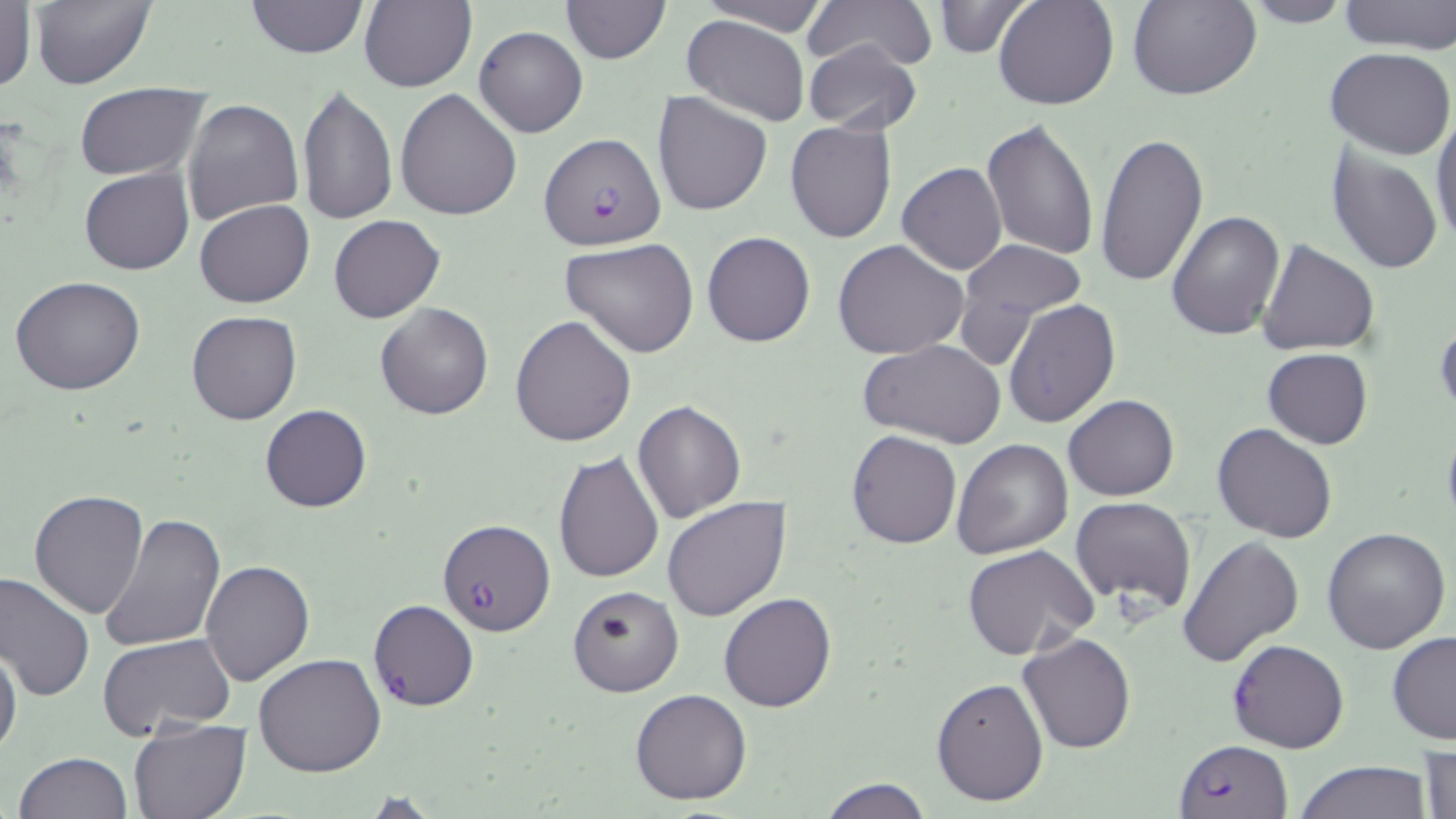

{
  "slide_level_diagnosis": "Plasmodium falciparum",
  "uninfected_red_blood_cell_locations": "approximate bounding boxes as [x1, y1, x2, y2] in pixels: [28, 0, 155, 89], [246, 0, 366, 58], [560, 0, 670, 64], [694, 0, 829, 34], [799, 0, 934, 71], [993, 0, 1119, 110], [1128, 0, 1260, 100], [1336, 0, 1456, 53], [357, 1, 477, 91], [1236, 1, 1356, 28], [0, 2, 36, 94], [930, 2, 1033, 58], [682, 14, 809, 126], [474, 26, 588, 137], [803, 39, 922, 134], [1325, 47, 1456, 161], [74, 82, 209, 182], [296, 82, 397, 226], [395, 88, 521, 221], [651, 91, 773, 216], [183, 98, 307, 226], [1431, 109, 1456, 248], [981, 117, 1099, 261], [785, 118, 898, 245], [1094, 133, 1209, 289], [1326, 148, 1442, 274], [897, 162, 1007, 275], [79, 167, 193, 275], [195, 200, 314, 308], [1167, 211, 1285, 340], [329, 214, 446, 324], [702, 230, 816, 347], [560, 238, 700, 357], [832, 238, 969, 360], [1257, 239, 1381, 355], [958, 240, 1085, 332], [11, 275, 147, 395], [1004, 299, 1122, 431], [375, 302, 493, 419], [186, 310, 302, 426], [510, 315, 639, 447], [1435, 319, 1456, 422], [861, 340, 1007, 449], [1263, 348, 1373, 448], [1063, 395, 1180, 502], [632, 399, 746, 524], [258, 405, 372, 513], [1212, 422, 1338, 543], [1441, 422, 1456, 533], [560, 424, 733, 564], [846, 429, 963, 548], [951, 437, 1075, 558], [554, 450, 665, 582], [28, 489, 148, 619], [662, 496, 792, 623], [1069, 496, 1197, 616], [99, 512, 226, 653], [1320, 527, 1450, 655], [1177, 533, 1305, 668], [963, 546, 1097, 662], [201, 558, 315, 686], [0, 572, 96, 701], [566, 583, 682, 697], [718, 592, 837, 711], [368, 599, 479, 712], [99, 632, 235, 739], [1017, 632, 1138, 753], [1387, 632, 1456, 744], [0, 644, 22, 759], [254, 652, 387, 776], [932, 679, 1049, 806], [629, 688, 753, 805], [128, 718, 252, 818], [1418, 743, 1455, 819], [13, 752, 132, 819], [1294, 760, 1435, 819], [819, 778, 932, 818], [358, 791, 442, 818]",
  "stain": "May-Grünwald-Giemsa",
  "field_of_view": "one of a larger specimen",
  "magnification": "1000x",
  "modality": "light microscopy",
  "plasmodium_falciparum_infected_red_blood_cell_locations": "approximate bounding boxes as [x1, y1, x2, y2] in pixels: [540, 133, 666, 250], [437, 516, 554, 636], [1226, 640, 1349, 753], [1173, 739, 1292, 819]",
  "image_size": "1456×819 pixels",
  "preparation": "thin blood smear"
}